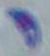
Photomicrograph. Captured at 1000x magnification. Toxoplasma gondii is shown.